Describe the morphology of the red blood cells.
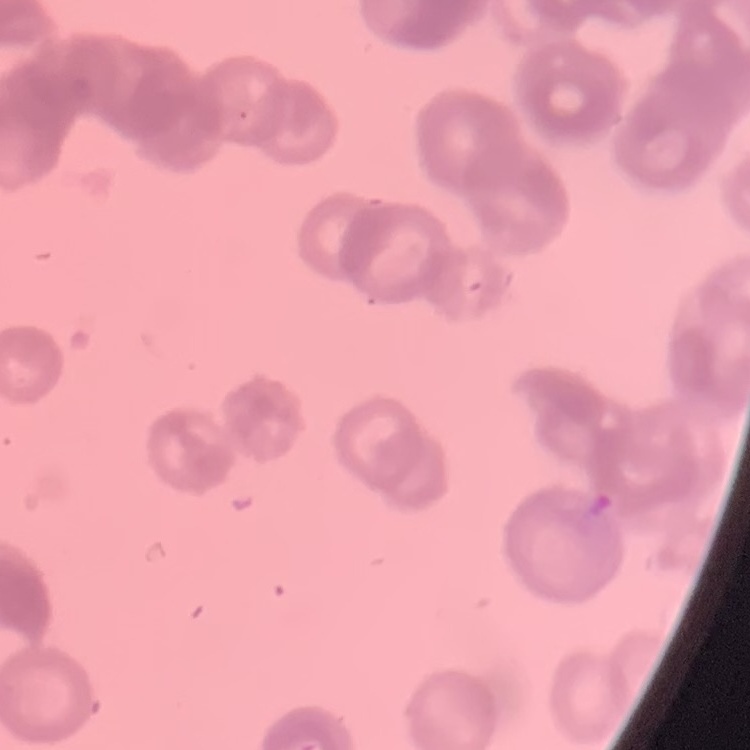

Rouleaux formation.

Summary:
  - Preparation: thin blood film
  - Image type: one tile cut from a larger photomicrograph
  - Stain: Field's or Giemsa